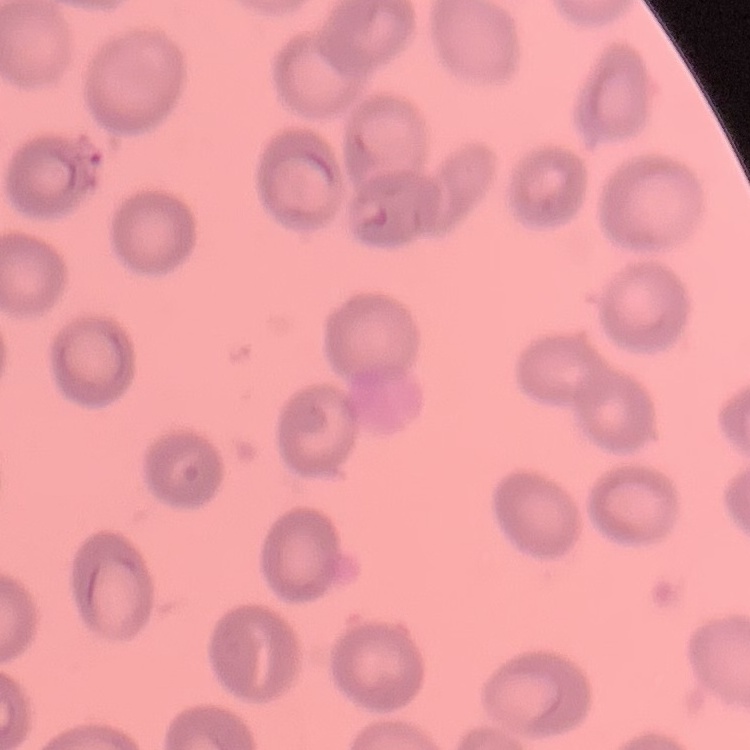
red blood cell morphology = no rouleaux formation
preparation = thin peripheral smear
stain = Field's or Giemsa
image type = one tile cut from a larger photomicrograph